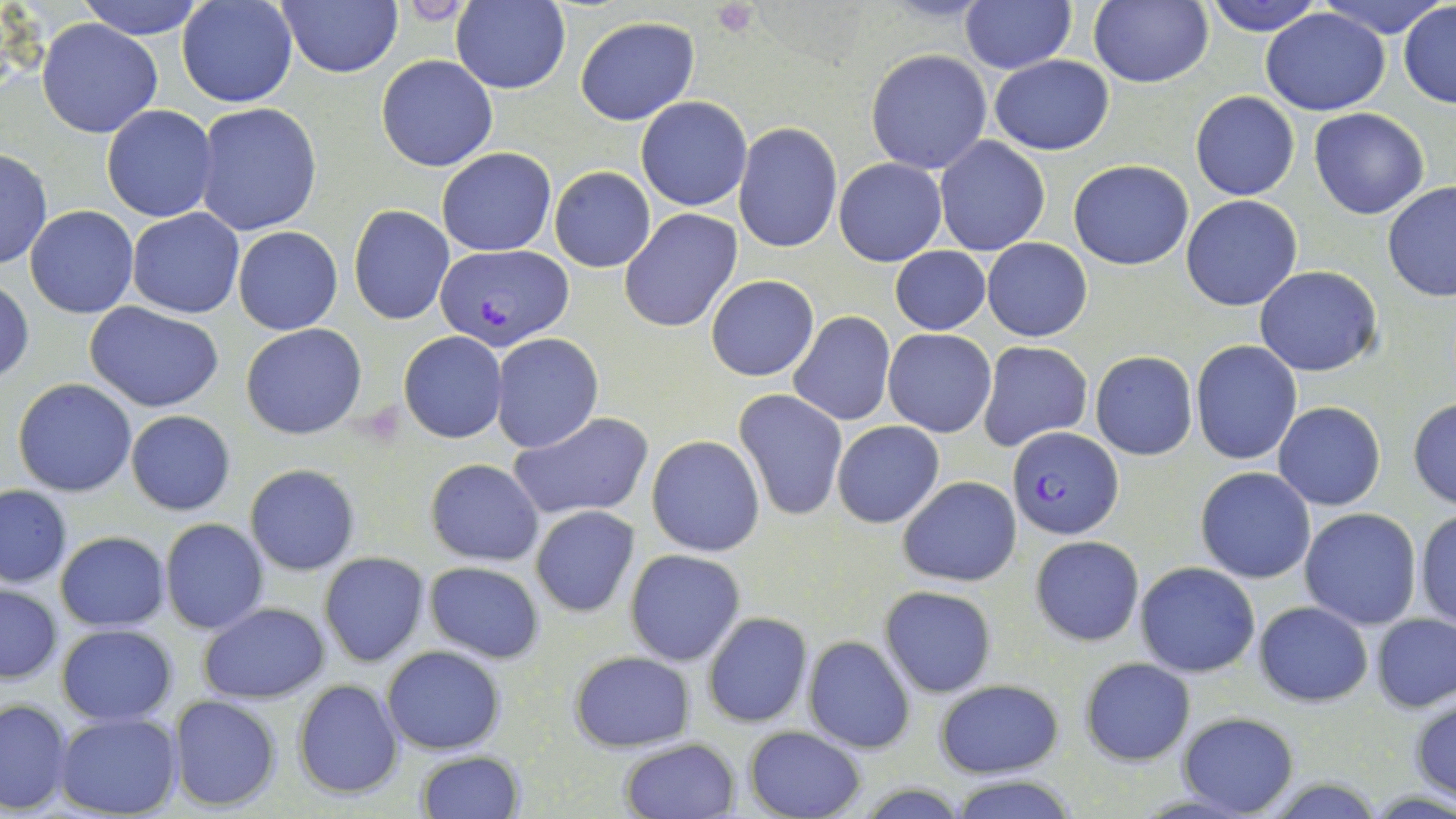

Summary:
  - Coordinate format: approximate bounding boxes as (x1,y1)-(x2,y2) corner pairs in pixels
  - Plasmodium falciparum-infected red blood cell locations: (433,244)-(574,350), (1009,425)-(1124,539)
  - Platelet locations: (713,1)-(760,38)
  - Uninfected red blood cell locations: (75,0)-(209,38), (177,0)-(299,107), (1205,0)-(1326,34), (1324,0)-(1441,34), (277,1)-(401,78), (451,1)-(571,93), (958,1)-(1075,73), (1087,2)-(1213,88), (1398,2)-(1456,109), (1261,8)-(1389,114), (574,17)-(698,125), (38,19)-(163,138), (865,49)-(994,174), (376,55)-(497,172), (989,55)-(1114,156), (1191,90)-(1300,200), (636,96)-(750,211), (194,103)-(322,236), (102,105)-(218,222), (1309,108)-(1431,219), (733,123)-(843,253), (934,136)-(1049,255), (437,148)-(555,257), (0,149)-(51,270), (834,157)-(947,266), (1068,158)-(1194,270), (549,167)-(656,272), (1382,181)-(1456,301), (1181,194)-(1304,311), (25,205)-(139,318), (347,205)-(454,325), (128,207)-(245,318), (621,208)-(742,332), (233,227)-(342,334), (983,237)-(1092,341), (891,246)-(992,335), (1254,265)-(1383,377), (705,274)-(819,382), (1,277)-(35,384), (84,303)-(226,415), (790,311)-(895,425), (241,323)-(367,440), (883,327)-(998,438), (398,331)-(508,444), (490,333)-(603,452), (1191,339)-(1302,465), (979,341)-(1093,451), (1090,351)-(1198,460), (12,378)-(138,497), (734,389)-(849,520), (1408,398)-(1456,509), (1273,401)-(1386,511), (125,410)-(235,515), (509,412)-(654,521), (832,420)-(944,528), (646,435)-(765,557), (426,459)-(543,566), (245,464)-(360,575), (1195,466)-(1317,583), (898,475)-(1021,587), (0,485)-(72,588), (530,505)-(640,617), (1299,508)-(1421,630), (1414,509)-(1456,629), (160,519)-(268,634), (54,532)-(171,631), (1030,535)-(1144,647), (625,549)-(744,666), (318,553)-(429,666), (424,562)-(544,663), (1134,562)-(1261,678), (1,584)-(62,684), (879,585)-(997,698), (1254,601)-(1372,707), (197,602)-(330,704), (701,612)-(813,727), (1372,613)-(1455,711), (57,623)-(177,726), (802,635)-(916,754), (381,645)-(506,754), (568,651)-(695,751), (1078,656)-(1195,765), (293,678)-(405,799), (933,679)-(1064,778), (168,694)-(283,811), (1410,695)-(1456,803), (0,699)-(73,814), (1176,711)-(1300,818), (54,713)-(180,818), (743,726)-(866,819), (618,738)-(740,819), (416,750)-(524,818), (946,773)-(1080,819)
  - Slide-level diagnosis: Plasmodium falciparum
  - Image size: 1456×819 pixels
  - Stain: May-Grünwald-Giemsa
  - Field of view: one of a larger specimen
  - Preparation: thin blood film
  - Modality: optical microscopy
  - Magnification: 1000x